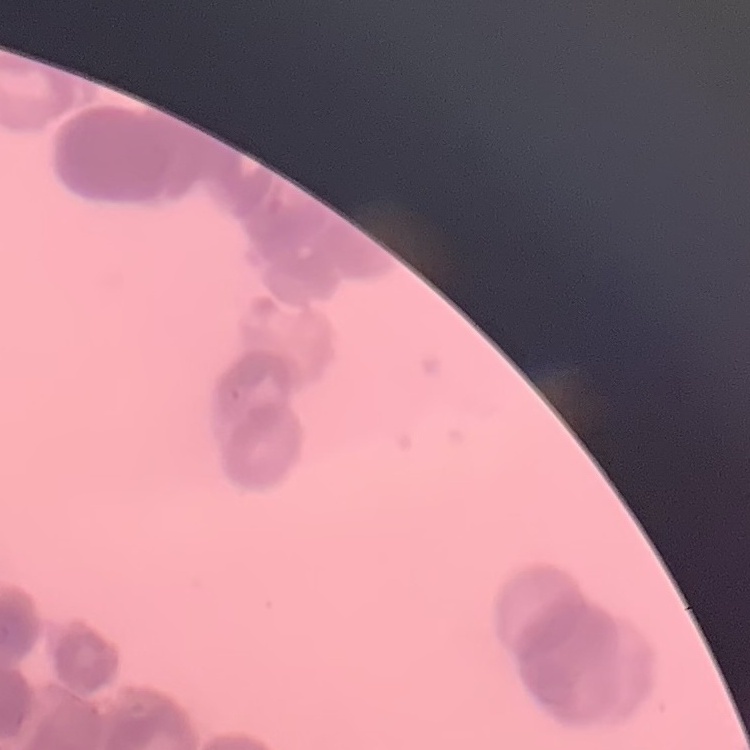

red_blood_cell_morphology: rouleaux formation
stain: Field's or Giemsa
image_type: square crop of a larger photomicrograph
preparation: thin peripheral smear